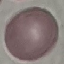
Result: no malaria parasites detected. Thin blood film. Giemsa-stained preparation. Automatically extracted cell patch, resized to 64 × 64 pixels. Photographed with a smartphone camera at the microscope eyepiece.